Report the malaria status of this cell.
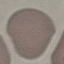

Uninfected.

Summary:
  - Preparation: thin smear
  - Stain: Giemsa
  - Image type: cell patch, automatically extracted from a larger field of view and resized to 64 × 64 pixels
  - Capture: smartphone camera at the microscope eyepiece